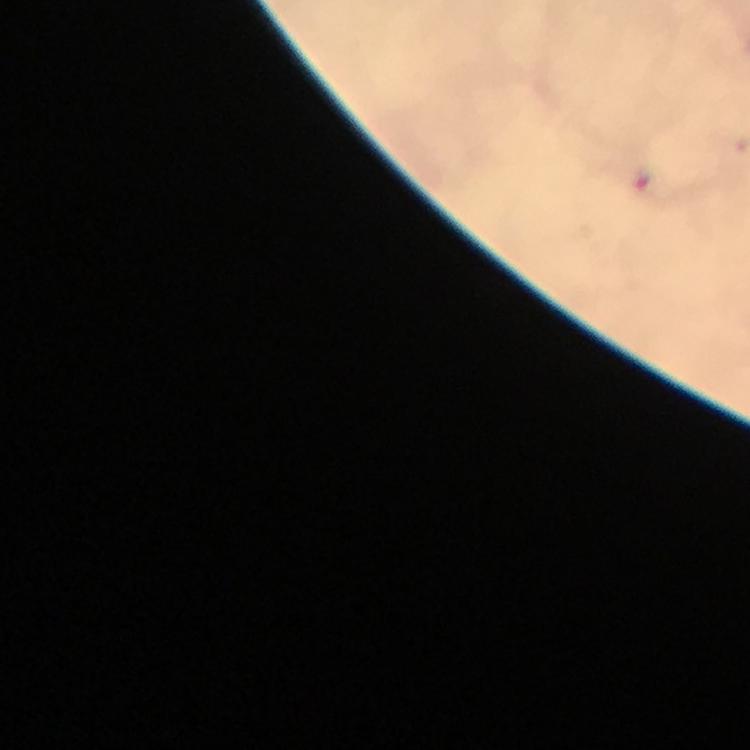

Approximate centers as {x, y} in pixels.
Summary:
  - Plasmodium parasite locations: {641, 180}
  - Context: from a malaria diagnostic workup
  - Stain: Giemsa
  - Image size: 750×750 pixels
  - Cropped from: a single field of view
  - Immersion oil: used
  - Preparation: thick blood smear
  - Capture: smartphone photograph through a microscope
  - Magnification: 100x